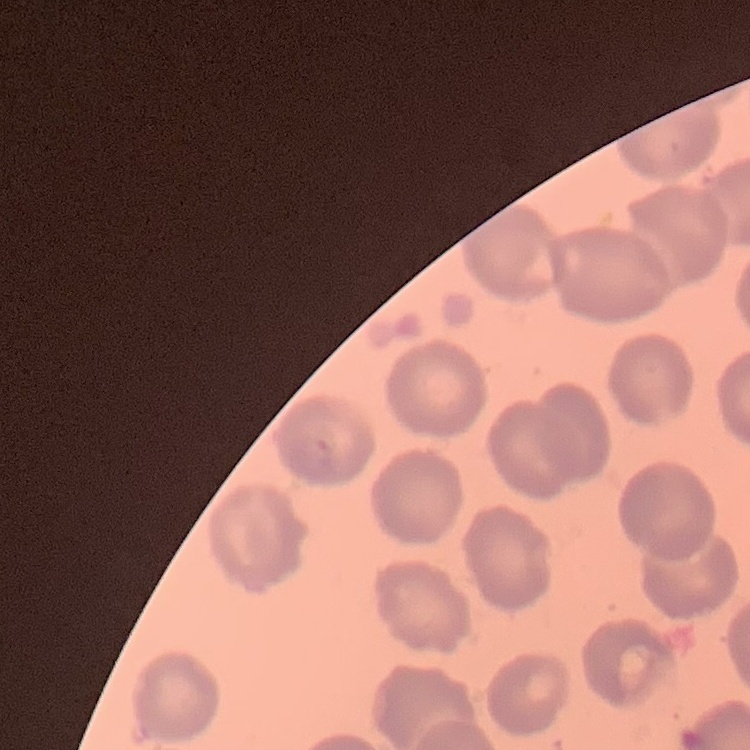

The red blood cells exhibit no rouleaux formation. Thin peripheral smear. Stained with either Field's or Giemsa. One tile cut from a larger photomicrograph.